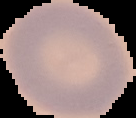
Summary:
  - Image size: 136×118 pixels
  - Image type: cell region segmented out of the field of view; surrounding area masked to black
  - Preparation: thin blood smear
  - Malaria status: uninfected